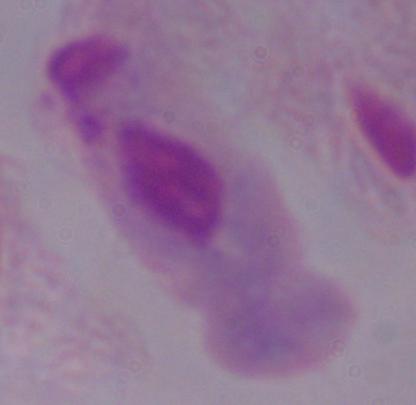

Summary:
  - Magnification: 1000x
  - Identification: trichomonad
  - Modality: photomicrograph